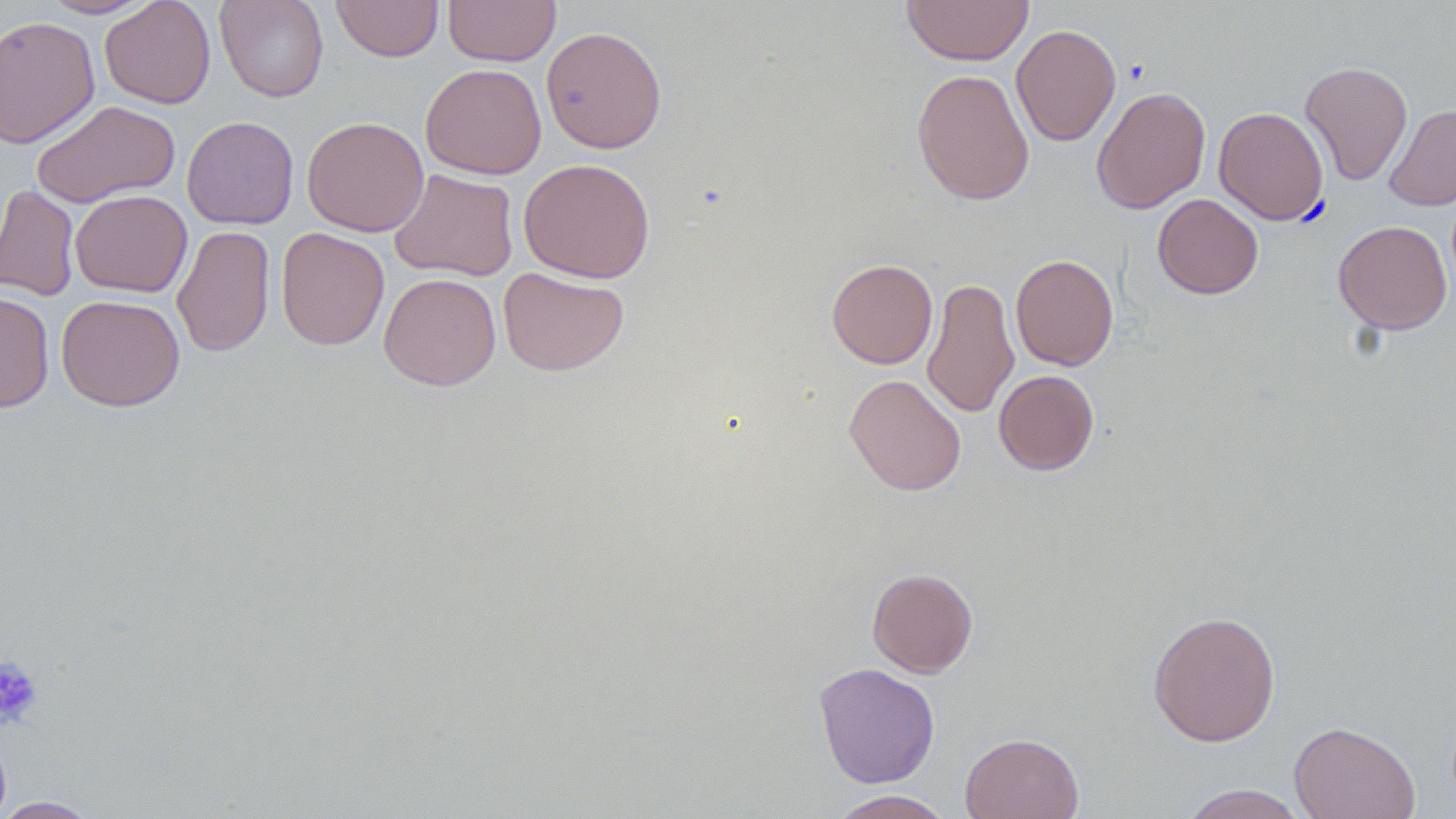

{
  "slide_level_diagnosis": "negative for blood parasites",
  "platelet_locations": "approximate bounding boxes as named x1/y1/x2/y2 corners in pixels: (x1=0, y1=655, x2=43, y2=728)",
  "preparation": "thin blood smear",
  "magnification": "1000x",
  "uninfected_red_blood_cell_locations": "approximate bounding boxes as named x1/y1/x2/y2 corners in pixels: (x1=40, y1=0, x2=155, y2=19), (x1=100, y1=0, x2=216, y2=109), (x1=215, y1=0, x2=329, y2=102), (x1=332, y1=0, x2=444, y2=62), (x1=443, y1=0, x2=561, y2=67), (x1=901, y1=0, x2=1034, y2=66), (x1=0, y1=15, x2=100, y2=149), (x1=1010, y1=23, x2=1121, y2=147), (x1=541, y1=25, x2=667, y2=153), (x1=1299, y1=60, x2=1413, y2=186), (x1=420, y1=63, x2=547, y2=179), (x1=912, y1=68, x2=1035, y2=206), (x1=1091, y1=85, x2=1211, y2=214), (x1=32, y1=99, x2=181, y2=208), (x1=1384, y1=103, x2=1456, y2=211), (x1=1213, y1=106, x2=1329, y2=225), (x1=181, y1=115, x2=299, y2=229), (x1=302, y1=116, x2=429, y2=236), (x1=518, y1=158, x2=655, y2=283), (x1=390, y1=169, x2=519, y2=281), (x1=0, y1=184, x2=80, y2=301), (x1=70, y1=189, x2=192, y2=297), (x1=1152, y1=193, x2=1264, y2=299), (x1=1333, y1=220, x2=1452, y2=335), (x1=172, y1=225, x2=276, y2=358), (x1=276, y1=228, x2=390, y2=350), (x1=1010, y1=254, x2=1119, y2=371), (x1=827, y1=258, x2=938, y2=369), (x1=498, y1=267, x2=629, y2=376), (x1=378, y1=272, x2=501, y2=391), (x1=922, y1=277, x2=1019, y2=419), (x1=0, y1=291, x2=55, y2=413), (x1=56, y1=295, x2=185, y2=411), (x1=994, y1=370, x2=1099, y2=475), (x1=844, y1=373, x2=966, y2=496), (x1=867, y1=567, x2=978, y2=678), (x1=1148, y1=610, x2=1281, y2=747), (x1=813, y1=662, x2=940, y2=789), (x1=1289, y1=720, x2=1421, y2=819), (x1=960, y1=732, x2=1084, y2=819), (x1=1178, y1=784, x2=1310, y2=819), (x1=829, y1=790, x2=954, y2=819), (x1=0, y1=797, x2=101, y2=818)",
  "modality": "light microscopy",
  "field_of_view": "one of a larger specimen",
  "image_size": "1456×819 pixels",
  "stain": "May-Grünwald-Giemsa"
}